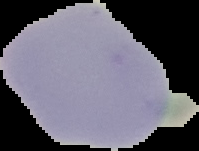

Summary:
  - Image size: 199×151 pixels
  - Preparation: thin blood film
  - Image type: segmented cell region on a black background
  - Malaria status: uninfected